State the preparation type.
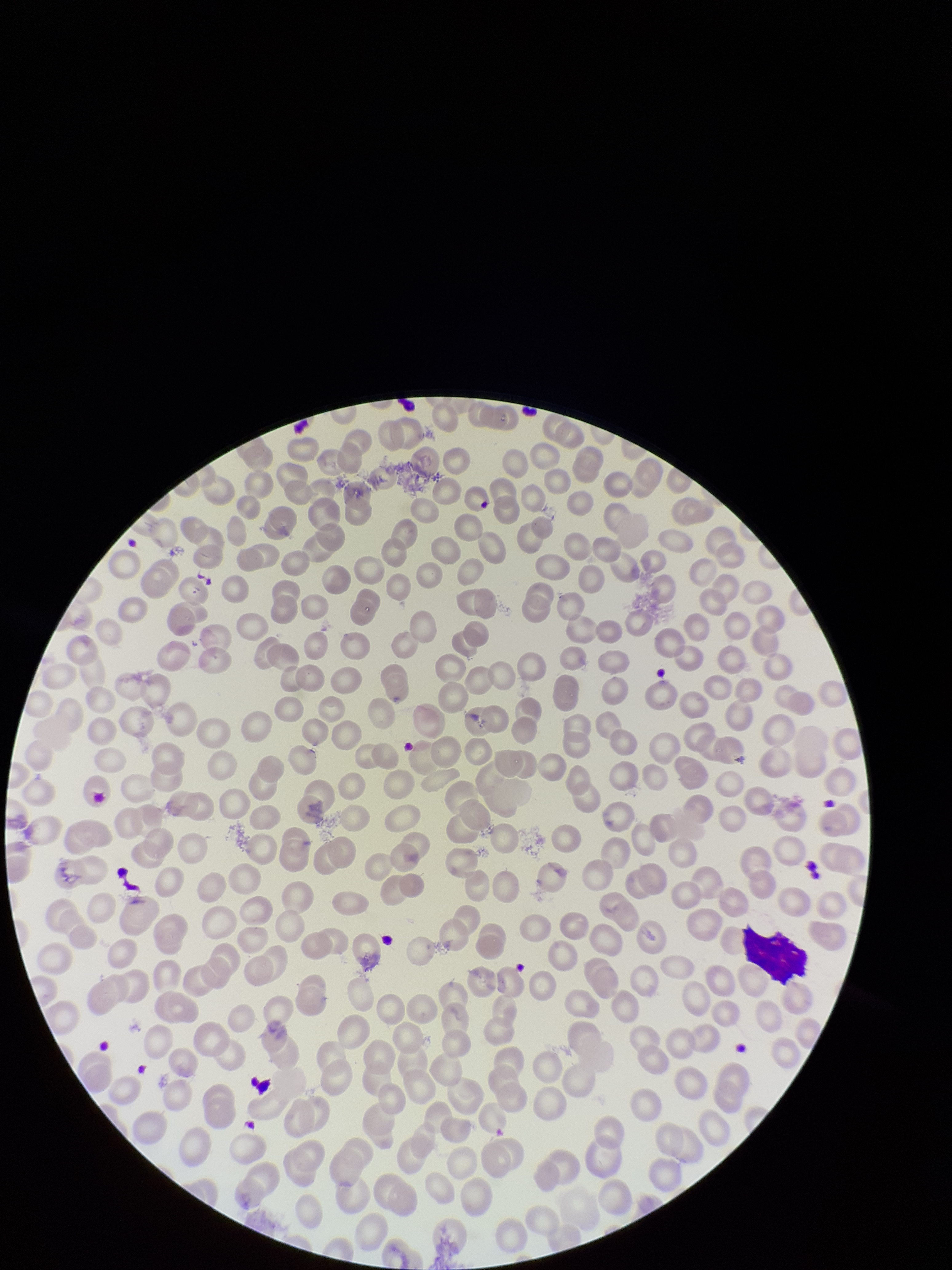

Thin.

Summary:
  - Image size: 952×1270 pixels
  - Patient malaria status: negative
  - Red blood cell count: 265
  - Capture: smartphone photograph through the microscope eyepiece
  - Stain: Giemsa
  - Field of view: one from this slide
  - Parasitized red blood cells: none seen
  - Parasitized red blood cell count: 0